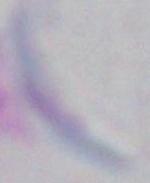

modality = micrograph
magnification = 1000x
identification = Toxoplasma gondii